Classify this cell by malaria status.
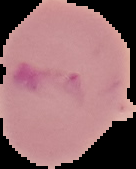
Uninfected.

preparation = thin blood smear
image type = segmented cell region with the area outside set to black
image size = 136×169 pixels